Locate every Babesia divergens-infected red blood cell.
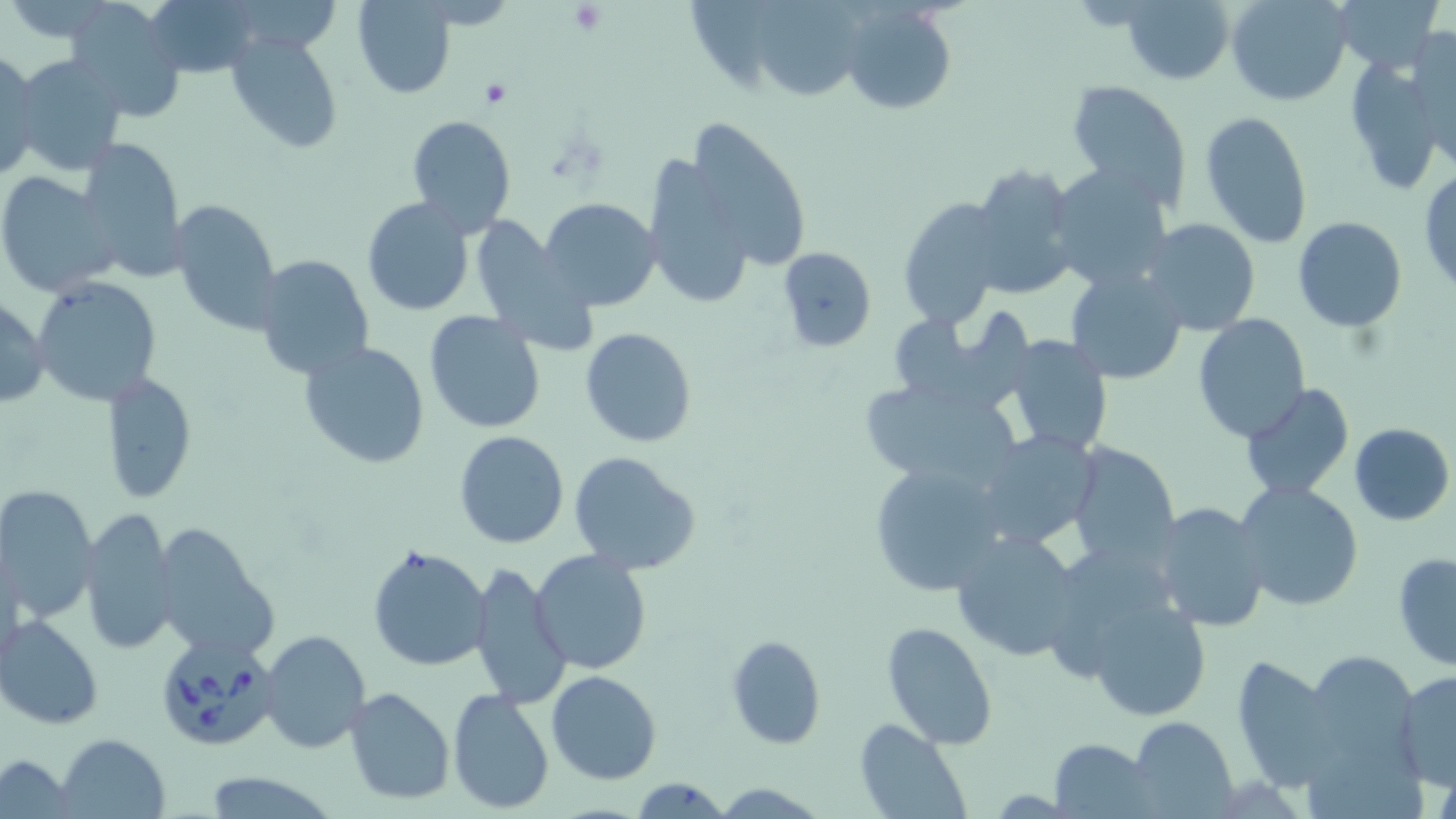

Approximate bounding boxes as (x1, y1, x2, y2) in pixels.
Babesia divergens-infected red blood cells: (164, 639, 287, 747).

Uninfected red blood cell locations: (141, 0, 258, 76), (759, 0, 858, 102), (1123, 0, 1233, 85), (1226, 0, 1351, 105), (1334, 0, 1442, 74), (354, 1, 455, 98), (687, 3, 775, 98), (65, 5, 187, 119), (843, 5, 956, 116), (1407, 24, 1456, 164), (226, 32, 344, 155), (0, 48, 41, 182), (10, 51, 129, 178), (1345, 59, 1442, 196), (1065, 81, 1193, 209), (1199, 110, 1316, 252), (405, 113, 516, 237), (684, 117, 811, 276), (76, 136, 188, 279), (644, 158, 755, 311), (968, 162, 1080, 299), (1047, 162, 1173, 291), (1419, 169, 1456, 297), (0, 171, 119, 298), (897, 196, 1007, 330), (361, 197, 477, 315), (170, 199, 282, 335), (539, 199, 661, 312), (468, 215, 592, 350), (1292, 216, 1407, 332), (1140, 218, 1262, 337), (776, 246, 878, 353), (254, 254, 374, 380), (1064, 267, 1188, 385), (33, 278, 160, 405), (0, 295, 49, 410), (884, 310, 1008, 413), (424, 311, 546, 433), (1193, 313, 1311, 443), (580, 327, 700, 449), (1006, 335, 1114, 457), (300, 340, 431, 469), (100, 371, 198, 505), (859, 379, 1025, 496), (1240, 385, 1355, 501), (1349, 422, 1454, 525), (454, 430, 568, 548), (976, 431, 1103, 551), (1063, 439, 1181, 568), (568, 450, 702, 576), (866, 462, 1009, 595), (1235, 482, 1364, 611), (0, 483, 99, 623), (1151, 502, 1270, 632), (80, 506, 180, 658), (150, 522, 279, 664), (950, 530, 1084, 661), (367, 544, 490, 671), (530, 549, 653, 677), (1059, 549, 1167, 677), (1393, 553, 1456, 670), (469, 561, 571, 708), (1085, 594, 1210, 721), (0, 614, 105, 729), (881, 622, 999, 751), (259, 629, 371, 753), (726, 635, 825, 749), (1301, 649, 1423, 784), (1229, 655, 1340, 794), (1394, 670, 1456, 789), (547, 671, 662, 784), (344, 688, 454, 804), (447, 688, 555, 815), (1131, 715, 1239, 818), (853, 719, 972, 819), (56, 733, 171, 818), (1051, 736, 1157, 817), (2, 756, 75, 815), (198, 770, 341, 818), (627, 776, 732, 817), (712, 780, 826, 817). Platelet locations: (568, 3, 606, 35), (478, 80, 511, 110). Slide-level diagnosis: Babesia divergens. May-Grünwald-Giemsa-stained preparation. Image is 1456×819 pixels. Light microscopy. Thin blood film. One field of a larger specimen. Captured at 1000x magnification.